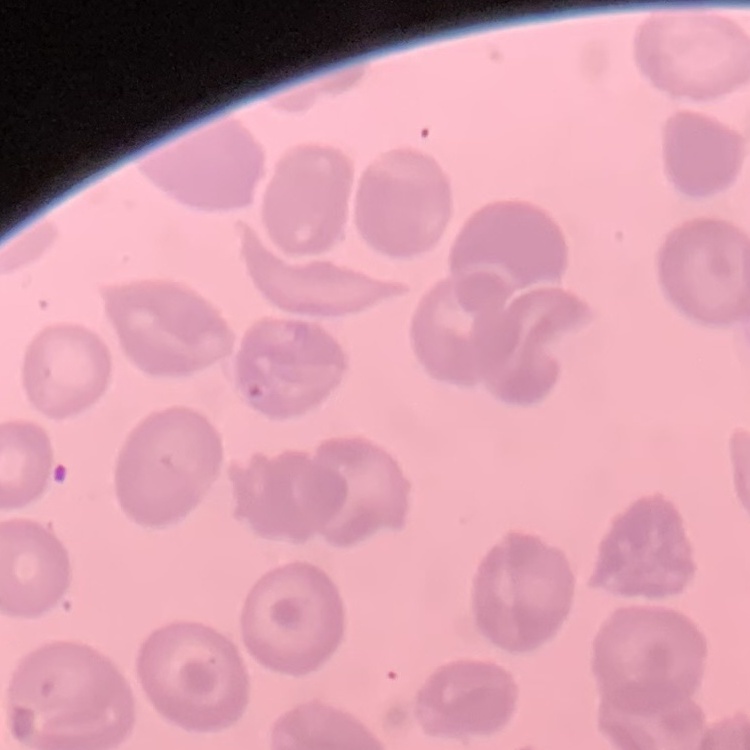
Summary:
  - Erythrocyte morphology: no rouleaux formation
  - Image type: square crop of a larger photomicrograph
  - Preparation: thin peripheral smear
  - Stain: Field's or Giemsa